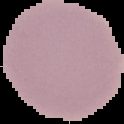

{
  "image_size": "124×124 pixels",
  "result": "no malaria parasites seen",
  "image_type": "segmented cell region on a black background",
  "preparation": "thin blood film"
}